Report the malaria status of this cell.
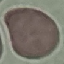

Uninfected.

{
  "image_type": "cell patch, automatically extracted from a larger field of view and resized to 64 × 64 pixels",
  "stain": "Giemsa",
  "preparation": "thin smear",
  "capture": "smartphone camera at the microscope eyepiece"
}